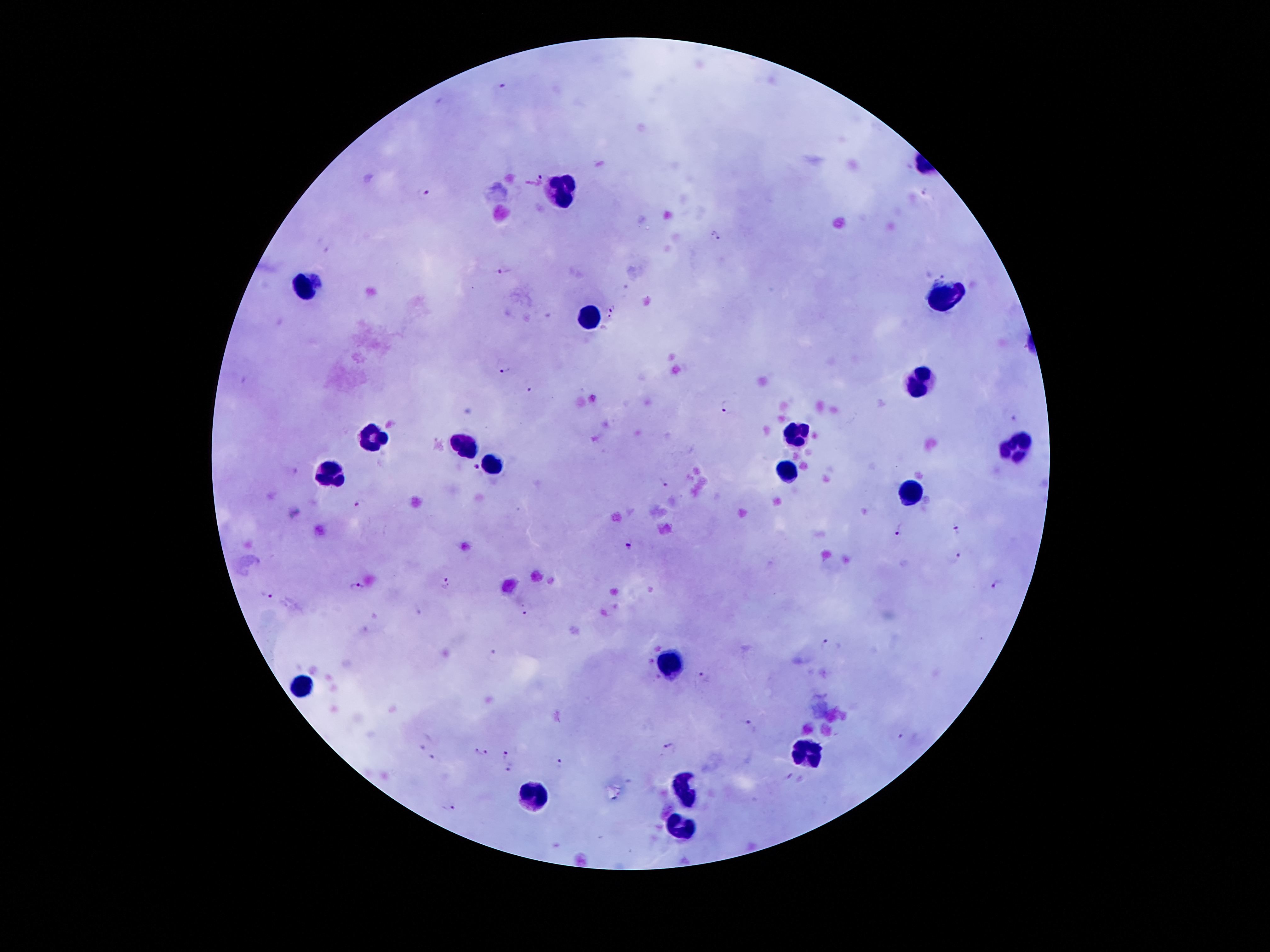 Approximate centers as {x, y} in pixels. Leukocyte locations: {560, 186}, {306, 285}, {945, 296}, {589, 317}, {921, 382}, {372, 437}, {794, 437}, {468, 447}, {1015, 447}, {493, 464}, {329, 474}, {784, 474}, {915, 494}, {669, 659}, {300, 685}, {802, 753}, {685, 788}, {531, 798}, {683, 826}. Plasmodium parasite locations: {504, 85}, {537, 178}, {925, 189}, {423, 193}, {715, 238}, {322, 245}, {504, 272}, {946, 276}, {612, 309}, {504, 368}, {530, 387}, {726, 406}, {1009, 416}, {476, 468}, {664, 483}, {360, 503}, {957, 528}, {901, 529}, {630, 544}, {958, 556}, {448, 582}, {999, 583}, {358, 585}, {266, 594}, {417, 610}, {524, 611}, {374, 617}, {826, 646}, {490, 656}, {703, 675}, {751, 725}, {902, 737}, {424, 743}, {669, 748}, {482, 752}, {508, 755}, {436, 758}, {557, 761}, {511, 770}, {789, 778}, {450, 806}. Giemsa-stained preparation. Image is 1270×952 pixels. Thick blood smear. 100x magnification. Patient malaria status: positive for Plasmodium falciparum. Single field of view. Smartphone photograph taken through the microscope eyepiece.